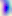
identification = Toxoplasma gondii
modality = micrograph
magnification = 400x